Comment on the morphology of the red blood cells.
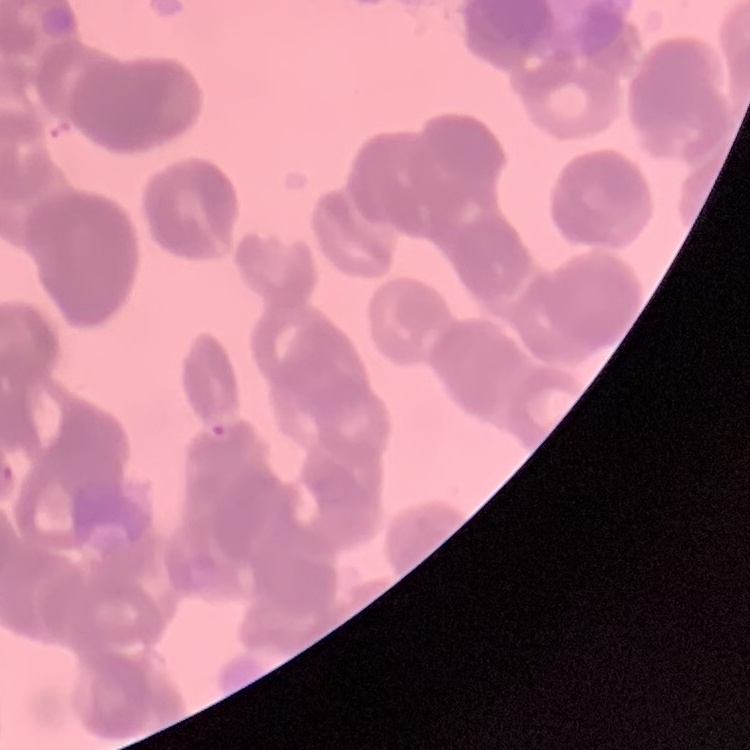
They show rouleaux formation.

Summary:
  - Stain: Field's or Giemsa
  - Image type: square crop of a larger photomicrograph
  - Preparation: thin peripheral smear